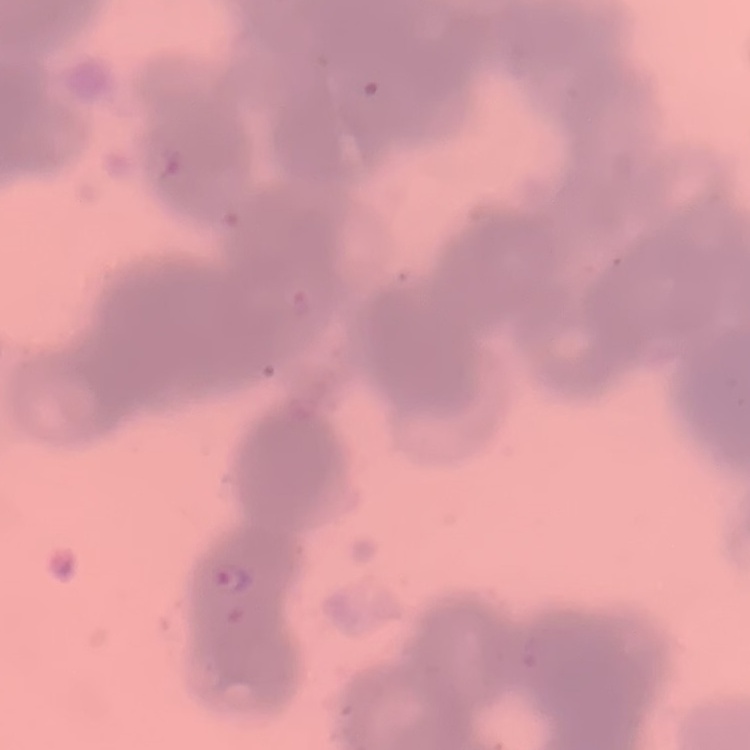

red_blood_cell_morphology: rouleaux formation
stain: Field's or Giemsa
image_type: one tile cut from a larger photomicrograph
preparation: thin blood film